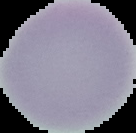

From a thin blood smear. Image is 136×133 pixels. Segmented cell region on a black background. Result: no malaria parasites seen.